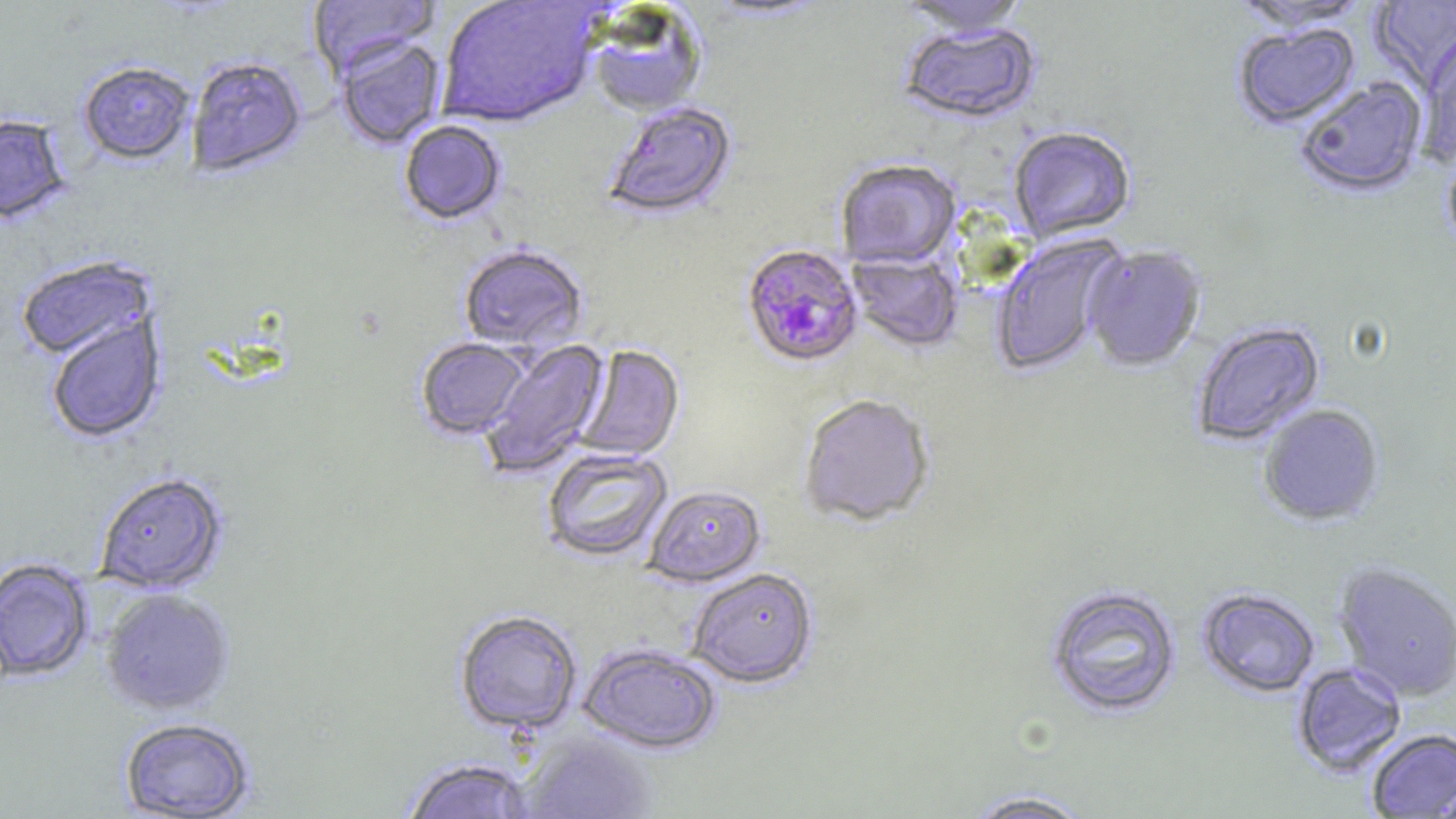
slide-level diagnosis = Plasmodium falciparum
modality = light microscopy
image size = 1456×819 pixels
magnification = 1000x
uninfected red blood cell locations = approximate bounding boxes as (x1, y1, x2, y2) in pixels: (307, 0, 438, 80), (438, 0, 604, 130), (701, 0, 832, 23), (897, 0, 1030, 39), (1370, 0, 1456, 93), (1231, 1, 1371, 34), (586, 5, 708, 118), (897, 24, 1041, 126), (1233, 24, 1361, 129), (335, 37, 445, 150), (1418, 37, 1456, 165), (187, 57, 306, 179), (79, 63, 195, 166), (1295, 78, 1428, 200), (602, 101, 738, 220), (0, 115, 72, 226), (399, 121, 506, 226), (1009, 128, 1136, 244), (836, 161, 961, 270), (990, 234, 1126, 376), (458, 246, 588, 354), (1084, 247, 1206, 371), (847, 250, 963, 353), (16, 257, 157, 362), (46, 315, 166, 443), (1190, 321, 1325, 447), (416, 338, 530, 440), (479, 339, 611, 479), (574, 345, 685, 462), (798, 395, 934, 529), (1257, 405, 1385, 527), (541, 448, 672, 563), (95, 473, 228, 594), (644, 486, 766, 588), (0, 559, 93, 681), (1333, 563, 1456, 702), (688, 568, 818, 689), (1045, 584, 1182, 719), (101, 588, 235, 715), (1198, 588, 1319, 698), (454, 610, 583, 736), (579, 644, 721, 754), (1292, 662, 1406, 777), (118, 718, 255, 818), (1366, 729, 1456, 818), (516, 732, 657, 819), (401, 758, 534, 819), (962, 789, 1098, 818)
field of view = single
Plasmodium falciparum-infected red blood cell locations = approximate bounding boxes as (x1, y1, x2, y2) in pixels: (740, 244, 864, 370)
preparation = thin blood smear
stain = May-Grünwald-Giemsa